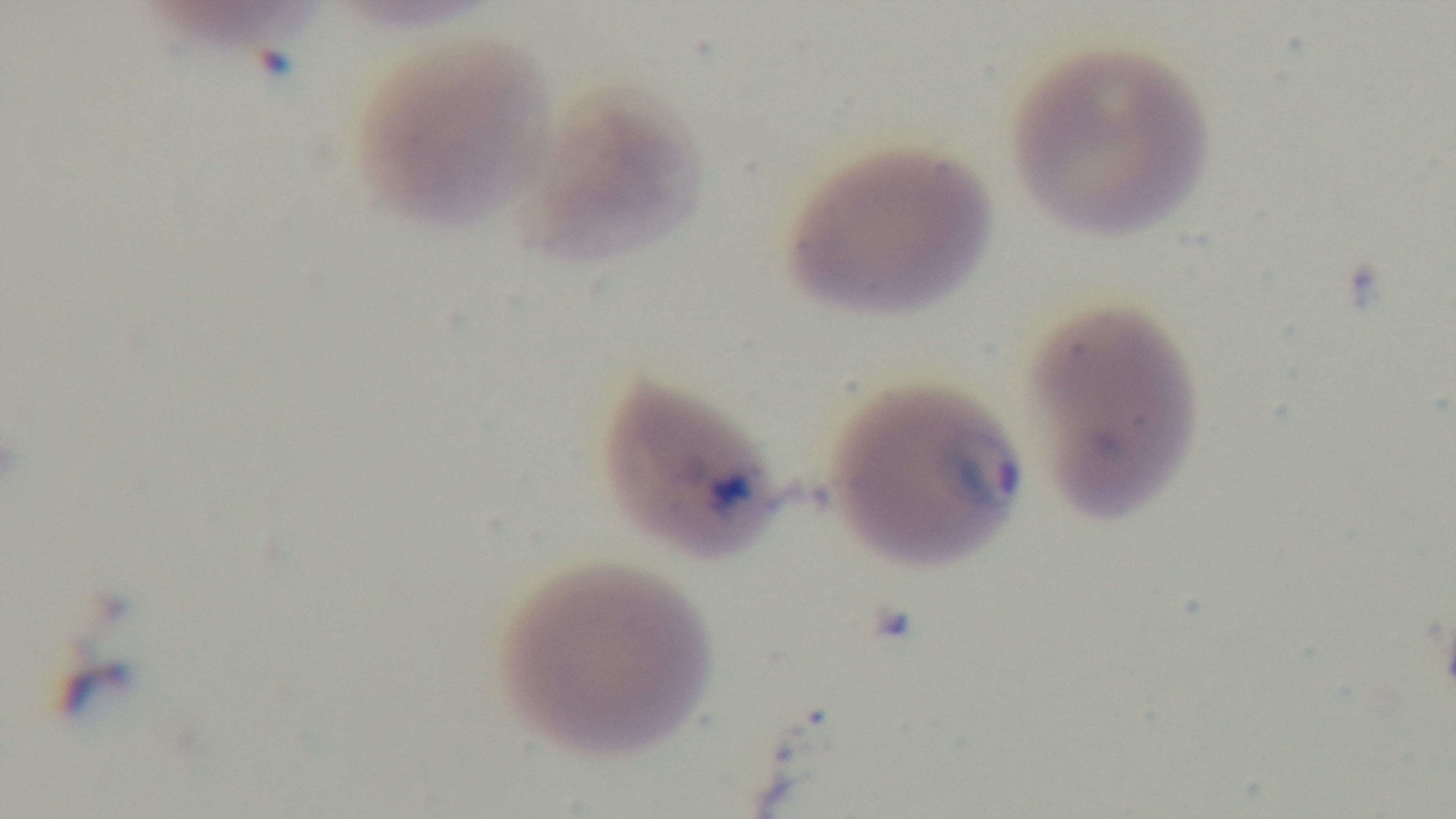 Mounted 4K digital camera. Preparation: thin. Malaria status: positive. Photomicrograph. Giemsa-stained. One field from the slide. Oil-immersion objective, 100x.